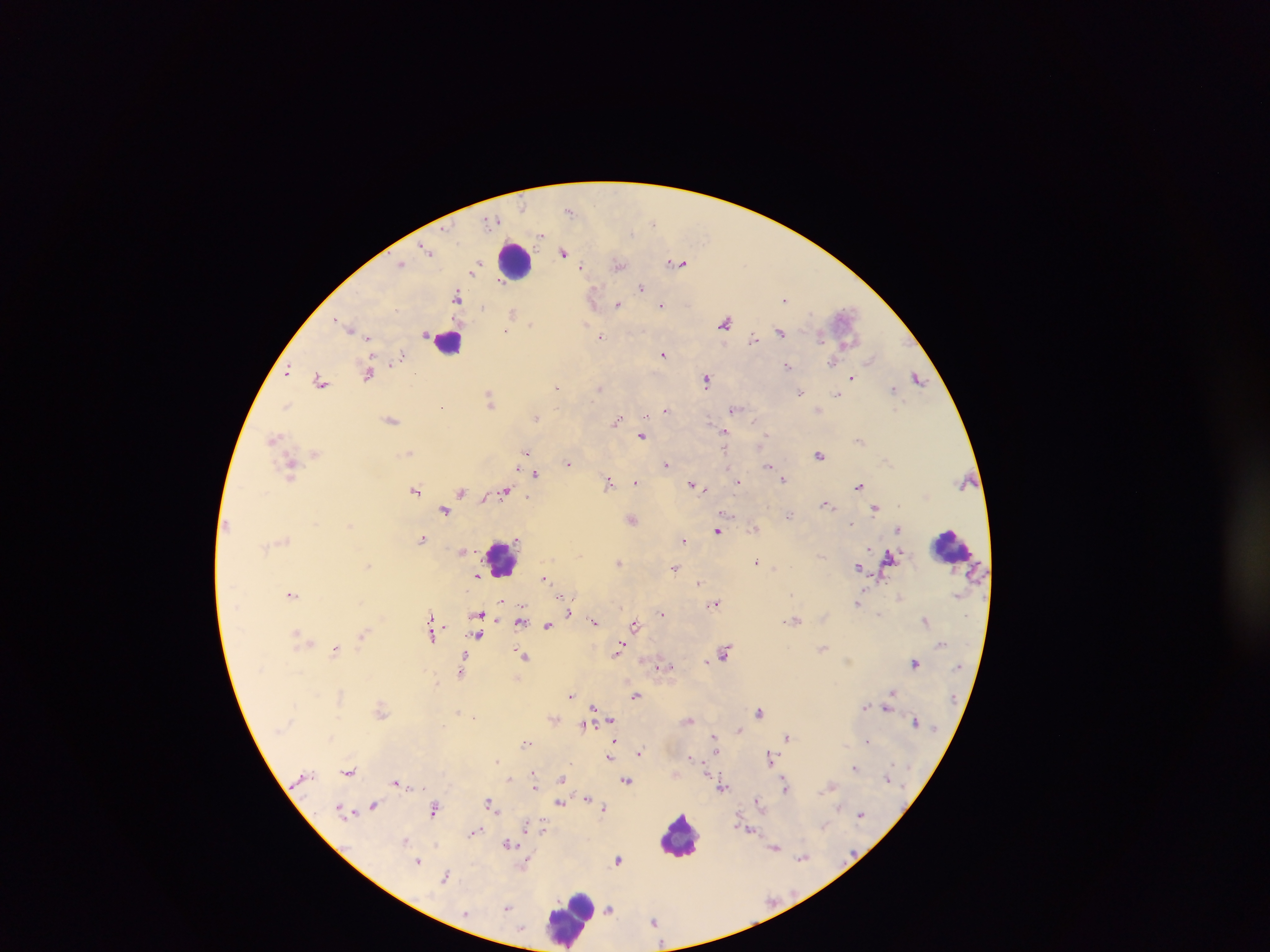 Approximate centers as x y in pixels. Malaria parasite locations: 570 210; 497 219; 652 222; 541 234; 427 249; 563 252; 430 253; 402 263; 478 263; 679 263; 618 264; 581 266; 472 272; 501 283; 642 288; 457 296; 593 298; 784 299; 618 304; 483 306; 662 306; 396 309; 512 313; 336 319; 725 321; 585 324; 531 325; 349 327; 356 330; 506 331; 780 331; 368 337; 601 337; 820 337; 754 338; 664 354; 403 355; 870 359; 832 362; 788 366; 288 372; 368 374; 415 374; 852 377; 917 377; 707 379; 321 381; 556 387; 600 388; 893 390; 800 394; 839 394; 490 398; 287 405; 442 407; 733 409; 666 410; 647 416; 537 417; 392 420; 618 420; 754 421; 724 432; 641 436; 765 436; 274 437; 315 453; 408 453; 526 453; 819 455; 567 462; 666 464; 728 466; 768 466; 290 467; 535 474; 737 476; 784 479; 636 482; 738 482; 609 483; 692 484; 858 485; 415 490; 505 490; 462 492; 827 504; 875 508; 444 510; 727 514; 790 514; 632 520; 851 524; 754 528; 899 529; 718 531; 422 538; 683 540; 466 550; 821 556; 888 558; 619 562; 757 562; 367 566; 675 567; 858 567; 478 575; 544 578; 699 582; 291 594; 564 598; 568 599; 503 601; 715 603; 858 603; 570 613; 662 613; 478 615; 880 615; 430 616; 925 620; 520 621; 595 622; 635 624; 547 625; 297 632; 363 634; 432 635; 478 635; 823 648; 335 649; 617 651; 725 651; 524 656; 706 661; 915 662; 664 666; 659 667; 461 669; 891 693; 340 695; 571 695; 636 695; 866 706; 594 707; 381 709; 885 710; 458 711; 759 711; 611 719; 689 720; 915 721; 585 727; 740 729; 713 736; 788 736; 867 740; 614 741; 526 743; 715 750; 640 752; 609 756; 691 756; 770 758; 497 760; 855 768; 349 771; 534 772; 707 775; 509 779; 561 779; 396 781; 626 781; 535 785; 831 786; 722 787; 785 788; 587 797; 758 801; 490 803; 560 803; 373 806; 604 807; 839 807; 434 808; 340 810; 860 814; 528 825; 824 826; 542 827; 751 830; 475 831; 406 840; 509 844; 775 847; 802 858; 617 859; 418 861; 527 864; 445 877; 507 908; 610 909; 654 920. Leukocyte locations: 514 261; 449 341; 951 546; 503 557; 681 835; 570 918. Sample from Ghana. Photographed through a microscope with a mobile-phone camera. Single field of view. Image is 1270×952 pixels. Thick blood film.